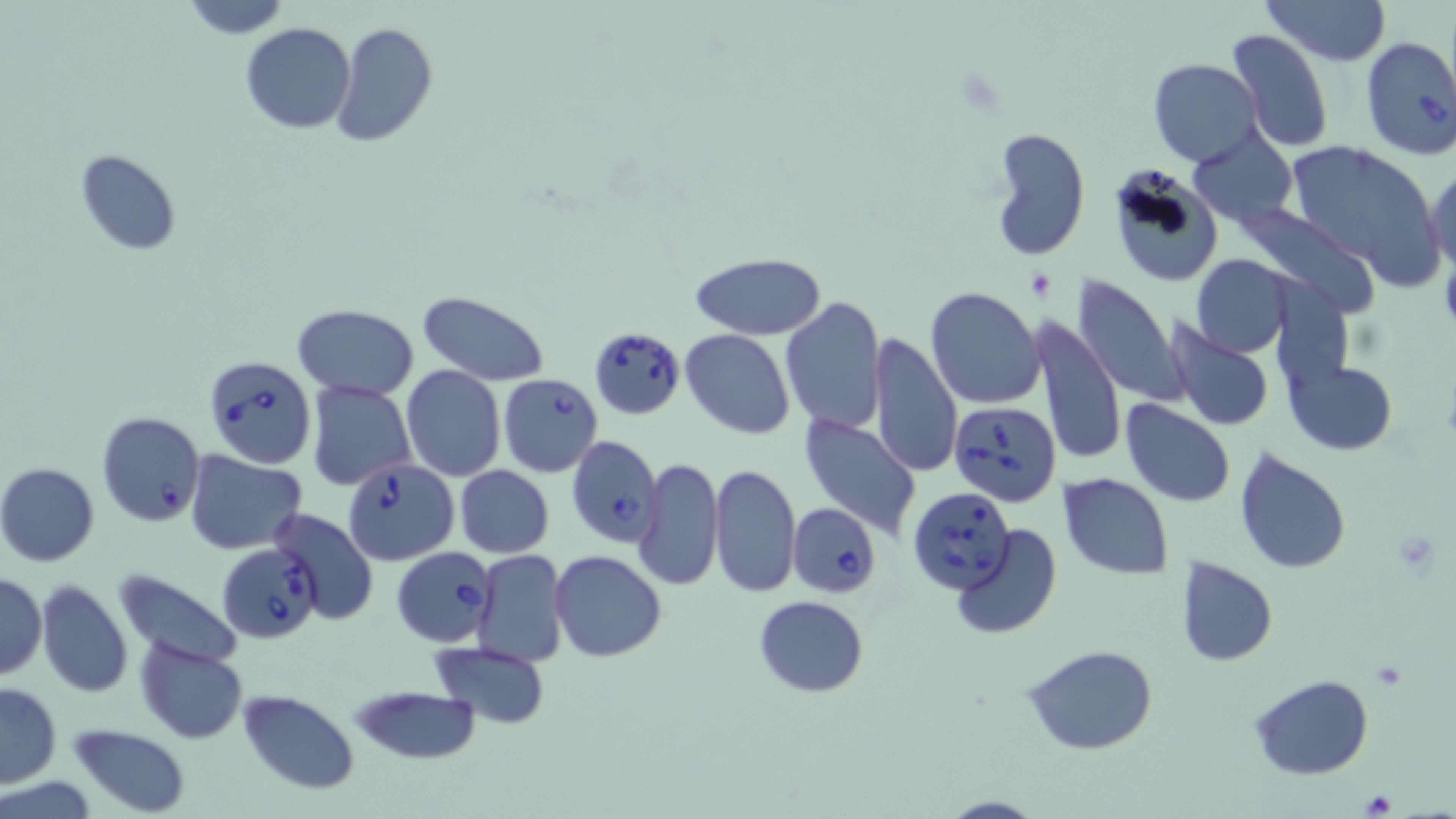

Summary:
  - Coordinate format: approximate bounding boxes as [x1, y1, x2, y2] in pixels
  - Platelet locations: [1392, 529, 1440, 573], [1370, 662, 1406, 691], [1363, 789, 1396, 815]
  - Babesia divergens-infected red blood cell locations: [1358, 33, 1456, 162], [589, 325, 685, 420], [207, 356, 314, 469], [498, 374, 603, 477], [949, 402, 1063, 506], [96, 412, 204, 525], [566, 435, 664, 548], [342, 458, 459, 566], [908, 489, 1015, 593], [787, 502, 879, 597], [219, 544, 320, 644], [391, 547, 498, 647]
  - Uninfected red blood cell locations: [178, 0, 293, 39], [1262, 0, 1392, 65], [333, 22, 438, 147], [241, 23, 357, 133], [1227, 30, 1333, 153], [1149, 58, 1262, 168], [989, 126, 1090, 260], [1189, 129, 1298, 229], [1282, 142, 1442, 283], [75, 148, 183, 255], [1426, 166, 1455, 274], [1116, 167, 1219, 283], [1232, 204, 1376, 316], [689, 253, 827, 339], [1191, 254, 1293, 358], [1070, 273, 1187, 407], [925, 286, 1044, 409], [417, 292, 550, 384], [778, 294, 887, 435], [292, 305, 419, 398], [1037, 314, 1126, 469], [1163, 321, 1275, 430], [680, 329, 795, 438], [869, 333, 963, 478], [1286, 360, 1398, 454], [400, 365, 506, 482], [306, 380, 416, 493], [1120, 401, 1236, 507], [798, 408, 923, 537], [1235, 447, 1354, 574], [187, 452, 308, 555], [636, 457, 725, 594], [0, 463, 99, 566], [709, 463, 802, 596], [455, 465, 553, 558], [1057, 473, 1174, 579], [269, 509, 380, 626], [952, 525, 1064, 640], [471, 549, 570, 668], [550, 550, 667, 662], [1174, 556, 1277, 668], [112, 570, 242, 672], [1, 572, 46, 680], [34, 580, 133, 698], [753, 596, 868, 697], [135, 637, 248, 743], [431, 641, 552, 731], [1023, 643, 1158, 757], [1250, 676, 1372, 780], [0, 682, 62, 788], [350, 683, 483, 766], [238, 689, 361, 795], [68, 723, 193, 817], [936, 794, 1047, 819]
  - Slide-level diagnosis: Babesia divergens
  - Preparation: thin blood smear
  - Modality: optical microscopy
  - Magnification: 1000x
  - Image size: 1456×819 pixels
  - Stain: May-Grünwald-Giemsa
  - Field of view: one of a larger specimen